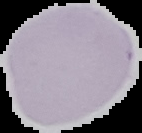
image type = cell region segmented out of the field of view; surrounding area masked to black
image size = 142×133 pixels
preparation = thin blood film
malaria status = uninfected